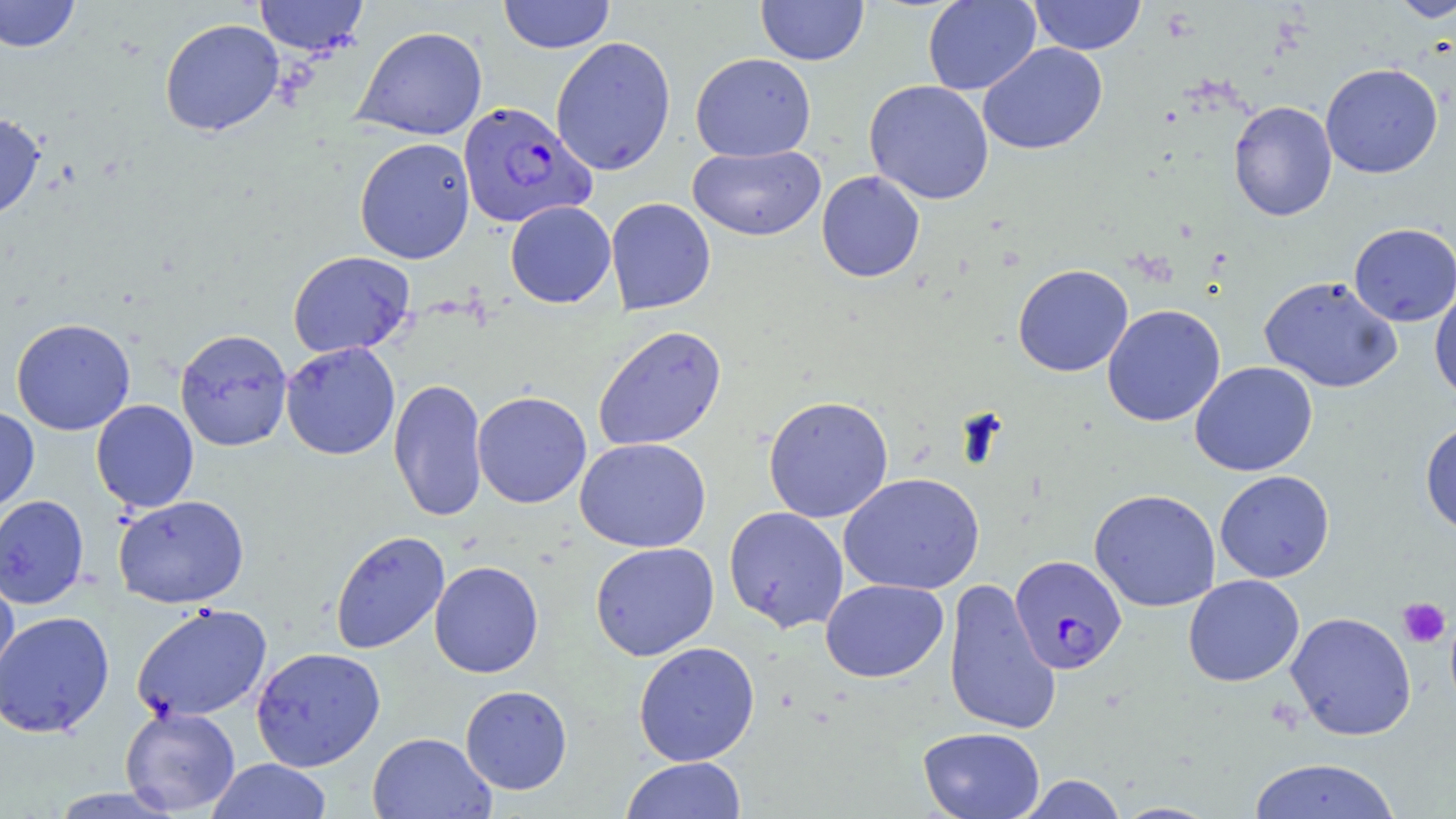 Approximate bounding boxes as named x1/y1/x2/y2 corners in pixels. Uninfected red blood cell locations: (x1=0, y1=0, x2=81, y2=53), (x1=253, y1=0, x2=369, y2=57), (x1=498, y1=0, x2=615, y2=54), (x1=756, y1=0, x2=869, y2=65), (x1=923, y1=0, x2=1041, y2=95), (x1=1028, y1=0, x2=1146, y2=55), (x1=1388, y1=0, x2=1456, y2=23), (x1=159, y1=18, x2=284, y2=136), (x1=353, y1=26, x2=488, y2=141), (x1=550, y1=36, x2=676, y2=176), (x1=978, y1=42, x2=1108, y2=155), (x1=690, y1=52, x2=816, y2=162), (x1=1320, y1=63, x2=1443, y2=179), (x1=864, y1=79, x2=994, y2=205), (x1=1228, y1=101, x2=1338, y2=221), (x1=0, y1=113, x2=45, y2=222), (x1=354, y1=137, x2=475, y2=264), (x1=688, y1=144, x2=826, y2=241), (x1=816, y1=170, x2=925, y2=283), (x1=605, y1=197, x2=716, y2=315), (x1=505, y1=200, x2=616, y2=308), (x1=1349, y1=222, x2=1455, y2=327), (x1=287, y1=251, x2=416, y2=359), (x1=1012, y1=264, x2=1134, y2=377), (x1=1259, y1=275, x2=1403, y2=393), (x1=1430, y1=282, x2=1456, y2=403), (x1=1101, y1=304, x2=1226, y2=427), (x1=11, y1=318, x2=135, y2=435), (x1=592, y1=324, x2=727, y2=452), (x1=174, y1=328, x2=293, y2=451), (x1=280, y1=341, x2=401, y2=460), (x1=1189, y1=361, x2=1318, y2=477), (x1=388, y1=377, x2=488, y2=523), (x1=472, y1=391, x2=591, y2=508), (x1=762, y1=395, x2=894, y2=523), (x1=91, y1=399, x2=199, y2=513), (x1=0, y1=406, x2=39, y2=514), (x1=1419, y1=420, x2=1456, y2=536), (x1=574, y1=437, x2=711, y2=553), (x1=1214, y1=470, x2=1335, y2=583), (x1=839, y1=472, x2=985, y2=595), (x1=1089, y1=488, x2=1221, y2=612), (x1=113, y1=494, x2=249, y2=609), (x1=0, y1=495, x2=90, y2=609), (x1=723, y1=506, x2=849, y2=633), (x1=330, y1=530, x2=450, y2=655), (x1=589, y1=542, x2=719, y2=661), (x1=429, y1=560, x2=544, y2=678), (x1=0, y1=565, x2=20, y2=696), (x1=1183, y1=574, x2=1305, y2=687), (x1=943, y1=577, x2=1060, y2=737), (x1=820, y1=578, x2=949, y2=683), (x1=131, y1=603, x2=272, y2=723), (x1=0, y1=610, x2=115, y2=738), (x1=1285, y1=611, x2=1417, y2=741), (x1=633, y1=641, x2=760, y2=766), (x1=250, y1=646, x2=386, y2=771), (x1=460, y1=685, x2=572, y2=794), (x1=120, y1=706, x2=240, y2=815), (x1=918, y1=727, x2=1045, y2=819), (x1=367, y1=732, x2=495, y2=819), (x1=620, y1=757, x2=747, y2=819), (x1=206, y1=758, x2=333, y2=819), (x1=1248, y1=758, x2=1403, y2=819), (x1=1017, y1=774, x2=1128, y2=818), (x1=46, y1=787, x2=184, y2=818). Platelet locations: (x1=1397, y1=597, x2=1451, y2=648). Plasmodium falciparum-infected red blood cell locations: (x1=457, y1=102, x2=595, y2=228), (x1=1010, y1=555, x2=1126, y2=674). Slide-level diagnosis: Plasmodium falciparum. Thin blood smear. One field of a larger specimen. May-Grünwald-Giemsa stain. Image is 1456×819 pixels. Optical microscopy. Captured at 1000x magnification.